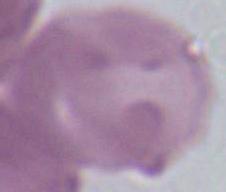

magnification = 1000x
modality = micrograph
identification = erythrocyte